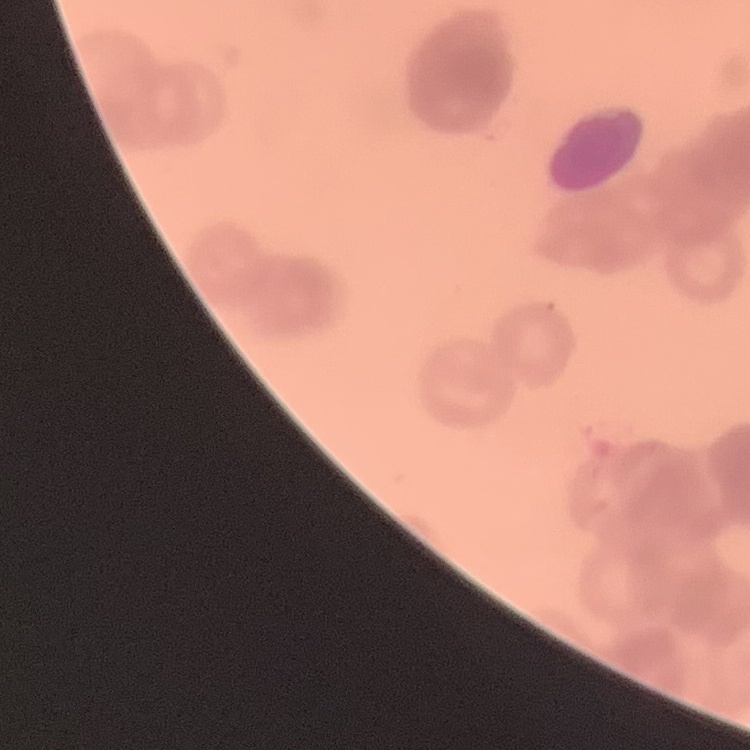 The red blood cells exhibit rouleaux formation. Thin peripheral smear. Square crop of a larger photomicrograph. Stained with either Field's or Giemsa.